Locate and identify every blood parasite.
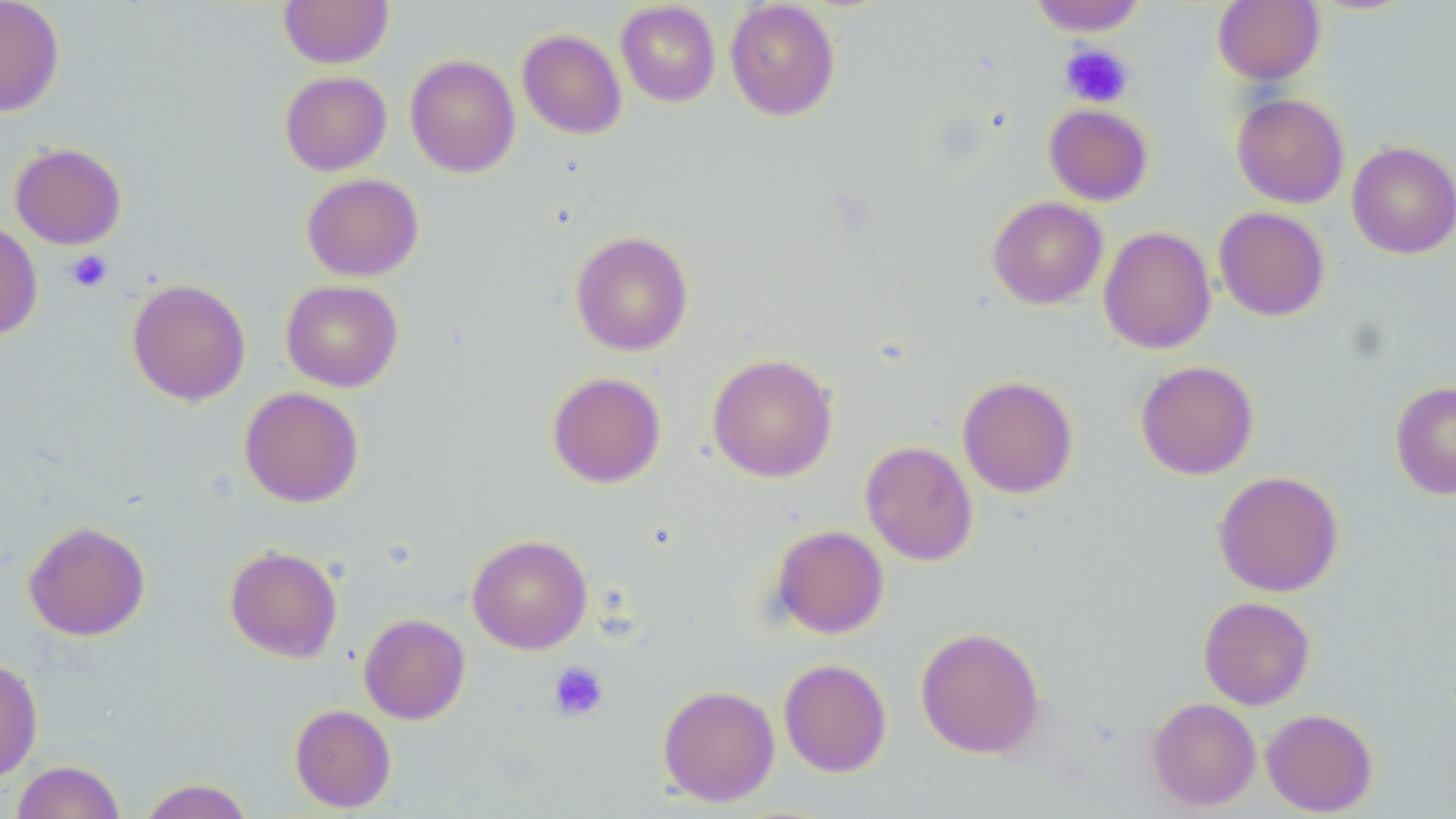
No blood parasites seen.

slide-level diagnosis = negative for blood parasites
uninfected red blood cell locations = approximate bounding boxes as [x1, y1, x2, y2] in pixels: [0, 0, 65, 117], [279, 0, 394, 68], [725, 0, 841, 121], [1028, 0, 1147, 36], [1212, 1, 1325, 85], [615, 2, 721, 107], [517, 28, 627, 140], [404, 54, 521, 178], [279, 71, 392, 176], [1231, 93, 1349, 208], [1044, 103, 1154, 206], [10, 141, 127, 250], [1347, 141, 1456, 259], [301, 173, 424, 281], [987, 196, 1108, 309], [1214, 206, 1330, 321], [0, 221, 43, 341], [1098, 226, 1216, 354], [569, 230, 694, 356], [126, 278, 251, 406], [280, 279, 404, 392], [707, 353, 838, 482], [1135, 360, 1259, 480], [546, 371, 667, 489], [957, 375, 1078, 499], [1390, 380, 1456, 500], [239, 386, 364, 508], [860, 440, 978, 565], [1212, 470, 1344, 597], [23, 520, 150, 641], [770, 524, 890, 639], [467, 534, 592, 654], [224, 544, 343, 663], [1198, 596, 1316, 710], [359, 613, 471, 725], [915, 626, 1045, 759], [0, 657, 43, 784], [778, 658, 892, 777], [658, 684, 780, 807], [1147, 696, 1261, 811], [289, 704, 397, 813], [1261, 708, 1378, 816], [11, 760, 125, 819], [137, 778, 254, 819]
stain = May-Grünwald-Giemsa
preparation = thin blood smear
modality = light microscopy
platelet locations = approximate bounding boxes as [x1, y1, x2, y2] in pixels: [1059, 43, 1134, 108], [65, 250, 113, 293], [548, 661, 609, 721]
field of view = single
magnification = 1000x
image size = 1456×819 pixels